Report the malaria status of this cell.
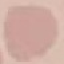

It is uninfected.

Summary:
  - Stain: Giemsa
  - Image type: cell patch, automatically extracted from a larger field of view and resized to 64 × 64 pixels
  - Capture: smartphone camera at the microscope eyepiece
  - Preparation: thin blood film